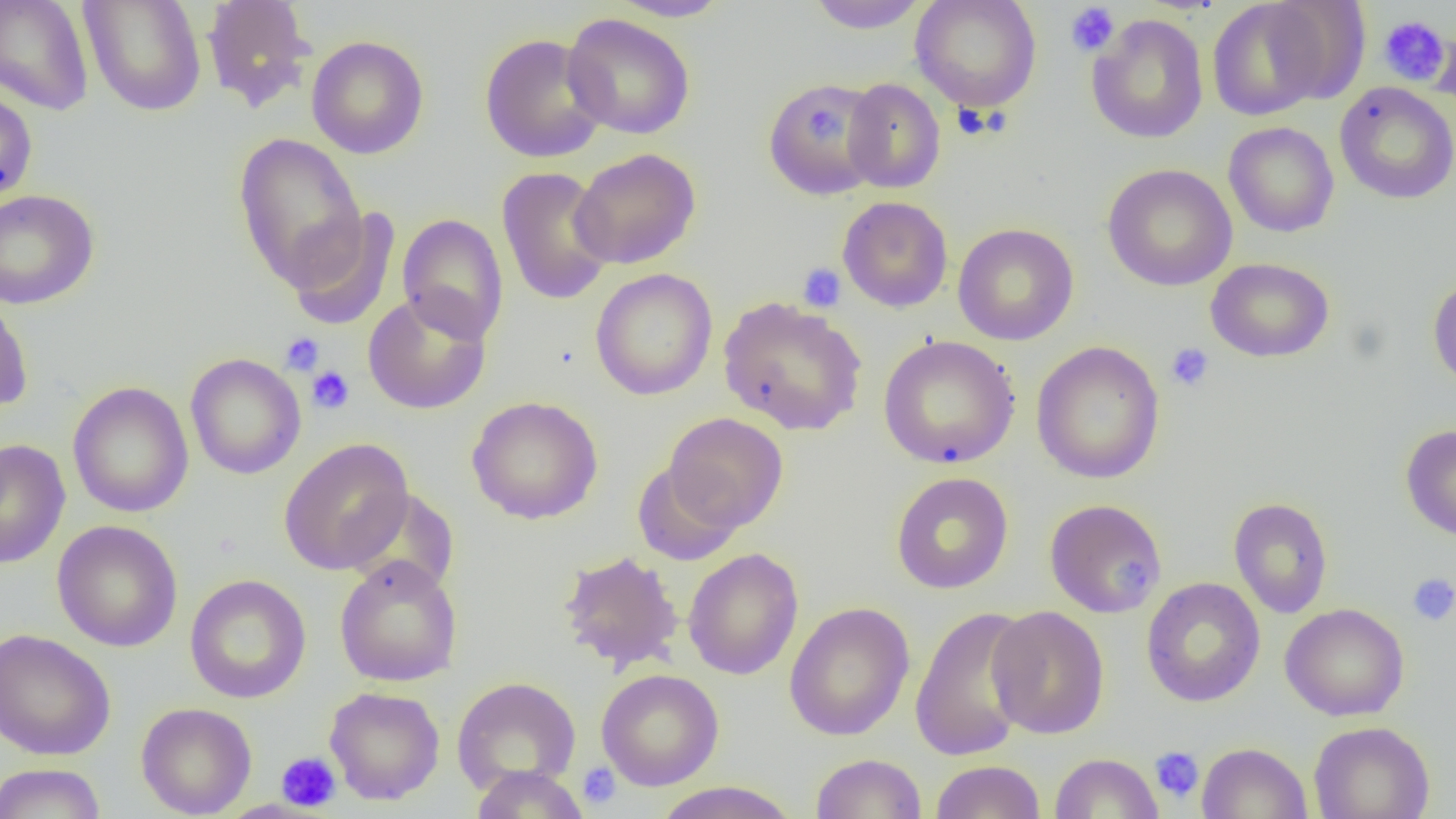

slide_level_diagnosis: no evidence of blood parasites
uninfected_red_blood_cell_locations: 'approximate bounding boxes as [x1, y1, x2, y2] in pixels: [0, 0, 94, 115], [79, 0, 207, 117], [607, 0, 735, 22], [805, 0, 930, 34], [910, 0, 1042, 112], [201, 1, 316, 112], [1207, 1, 1330, 121], [1266, 2, 1371, 104], [562, 13, 696, 140], [1088, 14, 1209, 144], [1376, 14, 1450, 84], [1428, 23, 1456, 117], [478, 32, 610, 163], [306, 35, 429, 159], [842, 78, 946, 193], [762, 79, 884, 201], [1334, 82, 1456, 204], [0, 86, 38, 206], [1223, 121, 1339, 238], [232, 132, 367, 290], [570, 148, 701, 270], [1102, 163, 1238, 291], [496, 167, 615, 305], [0, 189, 100, 310], [837, 196, 953, 313], [284, 207, 401, 330], [397, 213, 509, 344], [953, 223, 1079, 346], [1206, 257, 1335, 363], [590, 268, 718, 400], [1428, 275, 1456, 394], [0, 287, 35, 413], [362, 291, 492, 415], [717, 296, 868, 436], [878, 335, 1020, 469], [1031, 340, 1165, 485], [185, 353, 306, 479], [67, 381, 194, 518], [467, 395, 603, 524], [664, 412, 789, 532], [1400, 423, 1456, 541], [278, 437, 414, 575], [0, 438, 70, 569], [632, 462, 743, 567], [890, 471, 1013, 594], [343, 488, 460, 597], [1228, 497, 1333, 618], [1044, 498, 1167, 618], [52, 520, 183, 651], [683, 548, 803, 680], [558, 550, 684, 672], [334, 555, 463, 687], [184, 574, 311, 704], [1140, 577, 1265, 707], [784, 602, 915, 740], [1280, 603, 1410, 721], [909, 605, 1037, 761], [987, 605, 1110, 739], [0, 629, 116, 761], [596, 668, 724, 791], [451, 676, 581, 794], [324, 686, 445, 805], [136, 701, 257, 818], [1308, 721, 1435, 818], [1196, 742, 1313, 819], [1050, 752, 1163, 818], [811, 753, 927, 819], [930, 760, 1046, 818], [0, 762, 107, 819], [468, 765, 589, 818], [651, 781, 800, 819]'
field_of_view: single
preparation: thin blood film
platelet_locations: 'approximate bounding boxes as [x1, y1, x2, y2] in pixels: [1065, 3, 1120, 57], [1377, 16, 1450, 85], [808, 103, 846, 147], [951, 103, 997, 139], [798, 262, 847, 312], [280, 332, 325, 377], [1166, 342, 1214, 392], [307, 366, 355, 414], [1109, 561, 1146, 595], [1407, 573, 1456, 626], [1150, 746, 1204, 803], [276, 751, 342, 813], [576, 761, 622, 809]'
modality: optical microscopy
image_size: 1456×819 pixels
magnification: 1000x